Report the malaria status of this cell.
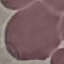
Uninfected.

Thin smear of blood. Giemsa-stained preparation. Automatically extracted cell patch, resized to 64 × 64 pixels. Acquired by smartphone through the microscope eyepiece.